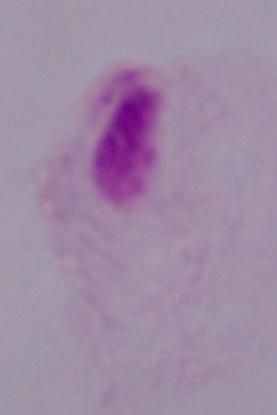 Photomicrograph. 1000x magnification. A trichomonad is seen.